Assess this cell for malaria.
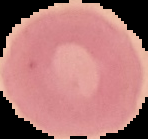
It is uninfected.

Image is 148×139 pixels. From a thin blood smear. Segmented cell region on a black background.